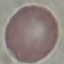
Summary:
  - Result: no malaria parasites seen
  - Image type: automatically extracted cell patch, resized to 64 × 64 pixels
  - Stain: Giemsa
  - Capture: smartphone camera at the microscope eyepiece
  - Preparation: thin blood film